Comment on the morphology of the erythrocytes.
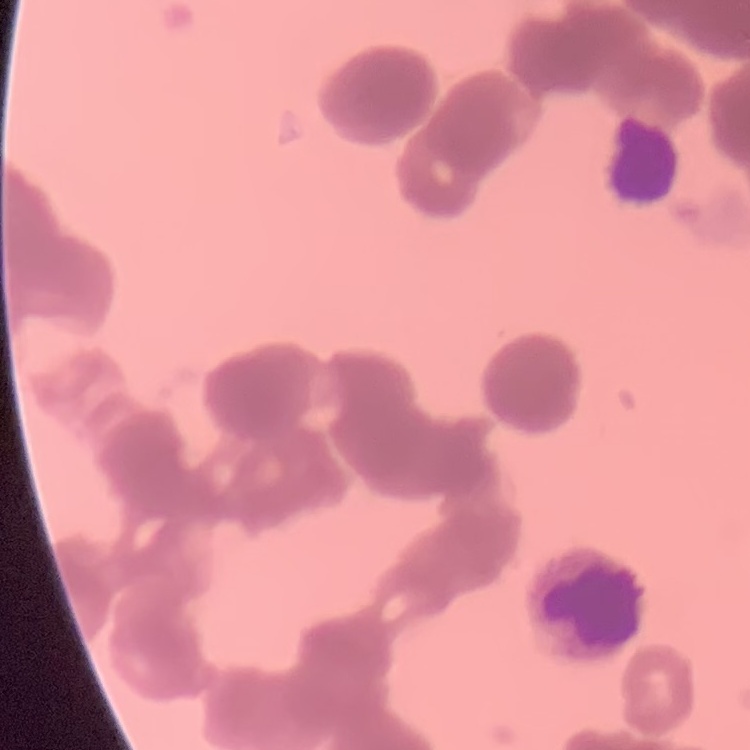
Rouleaux formation.

stain = Field's or Giemsa
preparation = thin blood smear
image type = square crop of a larger photomicrograph